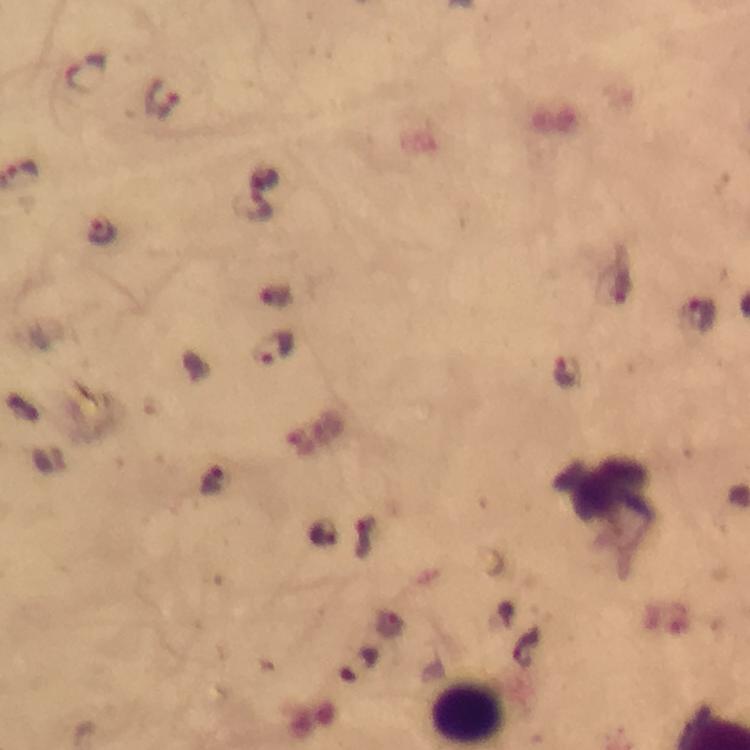

Approximate object centers, in pixels from the top-left corner. Malaria parasite locations: (x=85, y=73), (x=163, y=103), (x=255, y=208), (x=104, y=232), (x=697, y=317), (x=273, y=350), (x=568, y=372). Leukocyte locations: (x=610, y=502). A crop from one field of view. 100x magnification. Photographed with a smartphone mounted on the microscope. Thick smear. Immersion oil applied. From a malaria diagnostic workup. Giemsa stain. Image is 750×750 pixels.